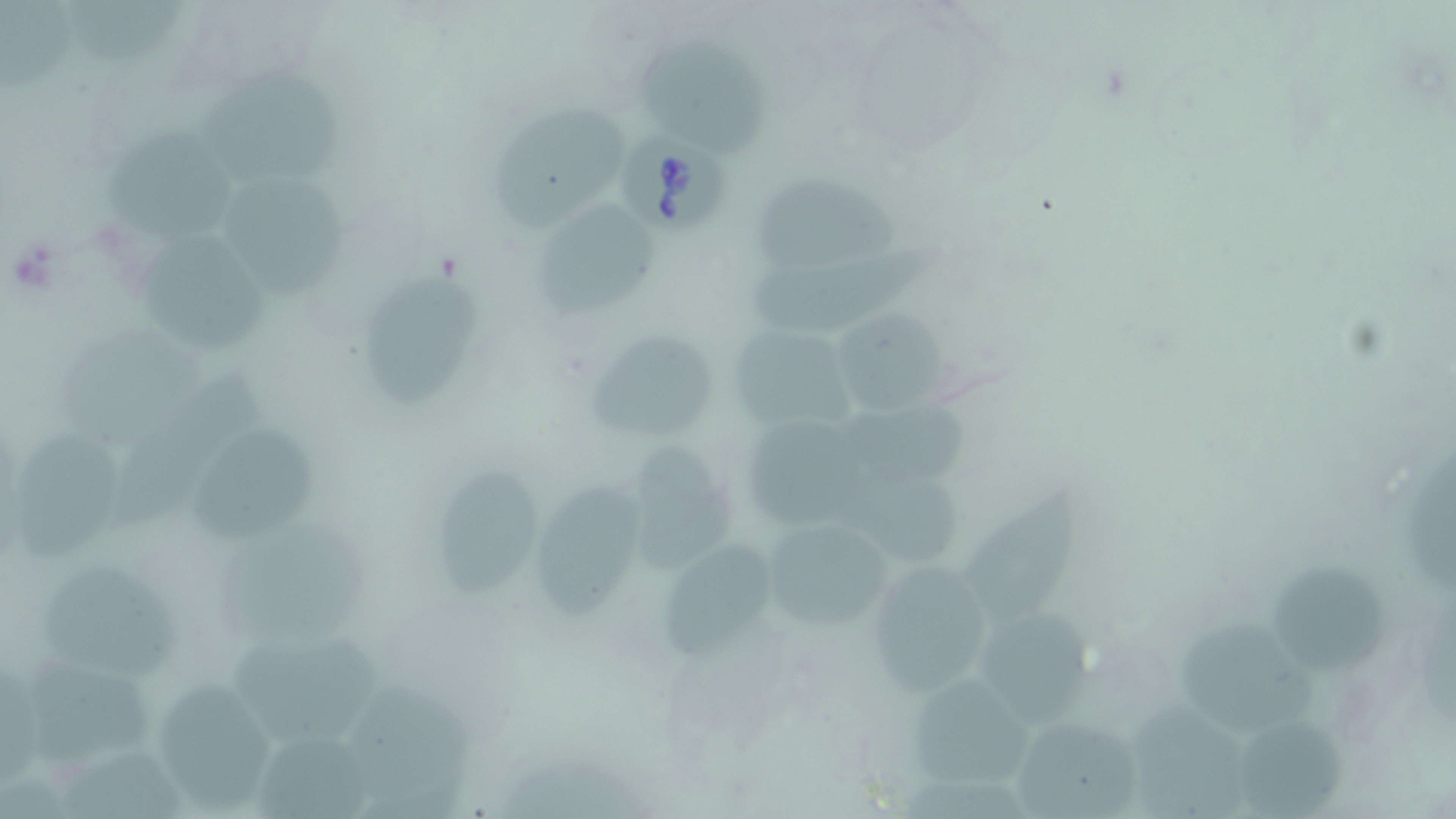

Approximate bounding boxes as (x1,y1)-(x2,y2) corner pairs in pixels. Uninfected red blood cell locations: (0,0)-(75,92), (61,0)-(183,65), (634,39)-(770,158), (200,70)-(338,186), (489,106)-(629,237), (103,129)-(233,242), (757,172)-(905,270), (223,173)-(347,295), (524,200)-(661,316), (142,233)-(266,350), (747,235)-(951,333), (362,267)-(484,406), (825,308)-(957,419), (726,320)-(855,435), (584,325)-(720,445), (109,373)-(262,531), (747,421)-(885,526), (192,422)-(317,546), (19,435)-(120,558), (619,442)-(739,571), (433,465)-(540,608), (827,467)-(963,570), (968,480)-(1080,626), (531,481)-(640,619), (759,519)-(894,634), (658,534)-(784,666), (1269,558)-(1387,675), (865,560)-(999,694), (38,563)-(181,680), (976,609)-(1101,726), (1177,620)-(1323,725), (233,636)-(382,742), (23,656)-(153,765), (904,674)-(1042,791), (146,676)-(278,813), (341,680)-(474,810), (1131,692)-(1266,819), (1010,713)-(1146,817), (1237,720)-(1349,819), (251,734)-(374,819), (65,748)-(198,819). Babesia divergens-infected red blood cell locations: (613,129)-(737,235). Slide-level diagnosis: Babesia divergens. May-Grünwald-Giemsa stain. Captured at 1000x magnification. Thin blood film. Single field of view. Optical microscopy. Image is 1456×819 pixels.